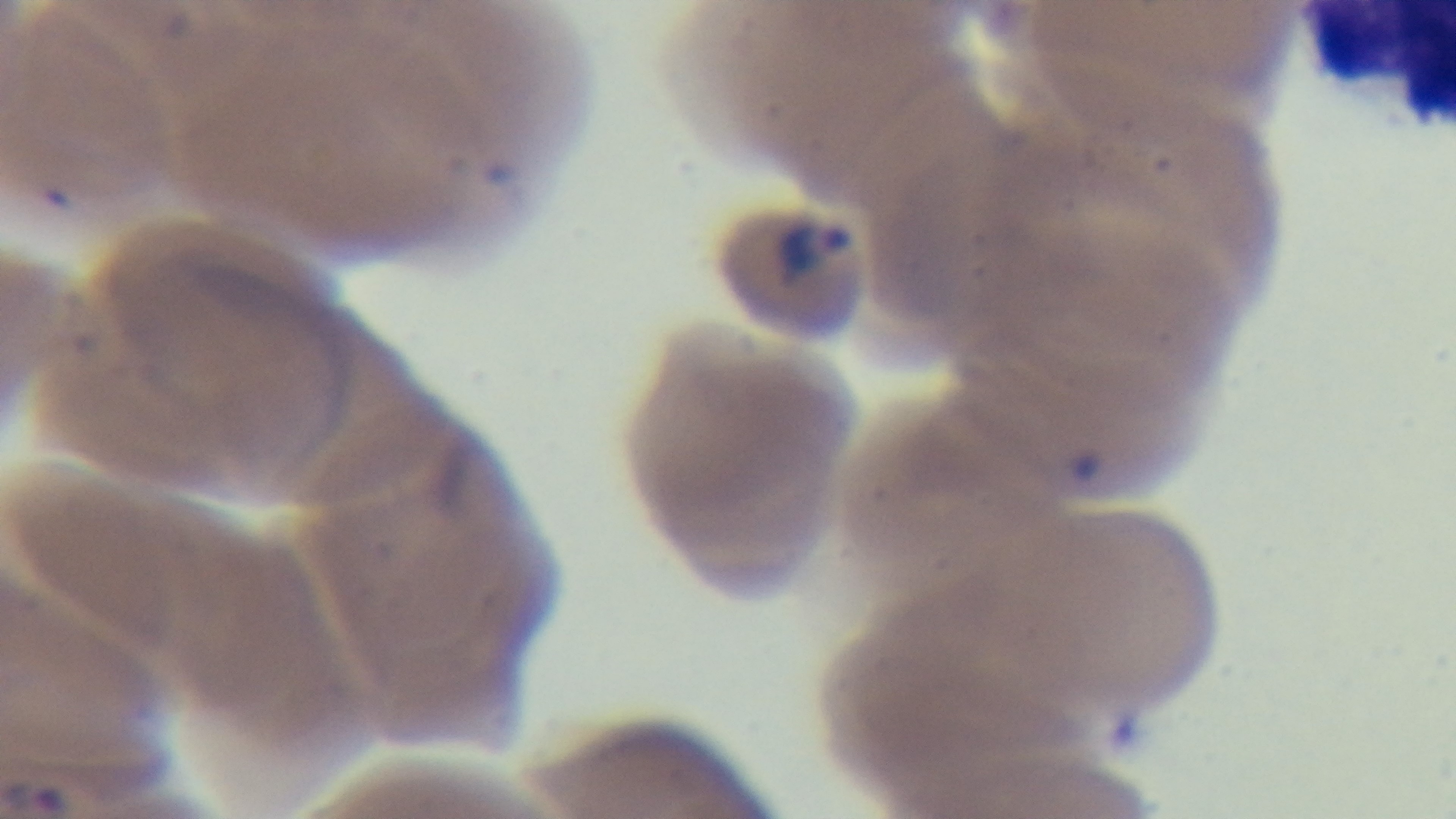

modality = light microscopy
stain = Giemsa
preparation = thin smear
objective = 100x oil immersion
malaria status = infected
field of view = one from the slide
capture = mounted 4K digital camera